Name the parasite shown.
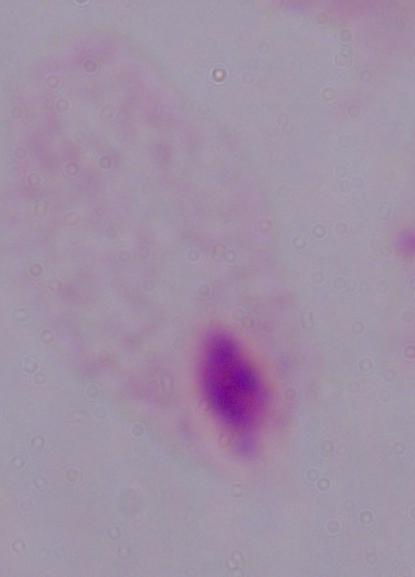
This is a trichomonad.

modality = photomicrograph
magnification = 1000x